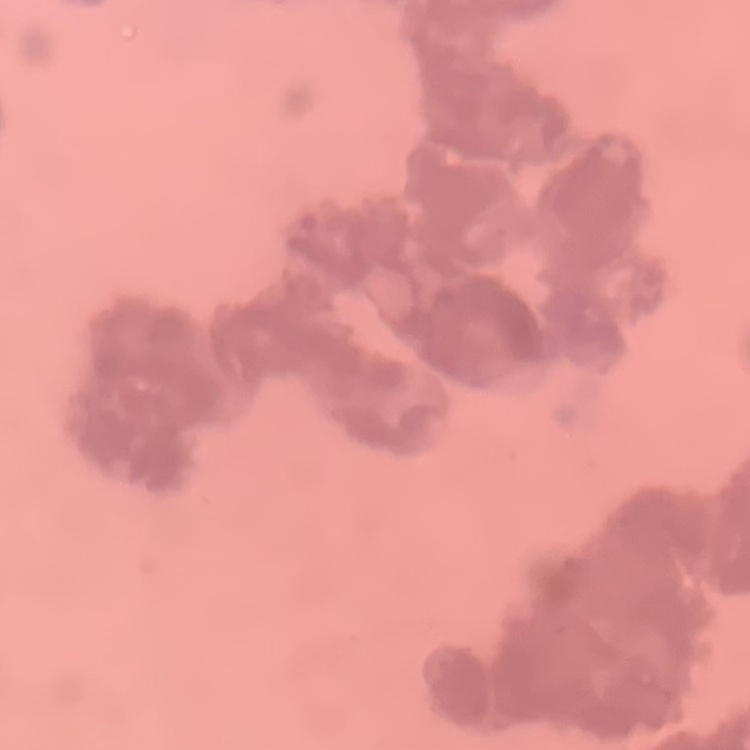
red blood cell morphology = rouleaux formation
image type = square crop of a larger photomicrograph
stain = Field's or Giemsa
preparation = thin blood film